Give the position of every malaria parasite.
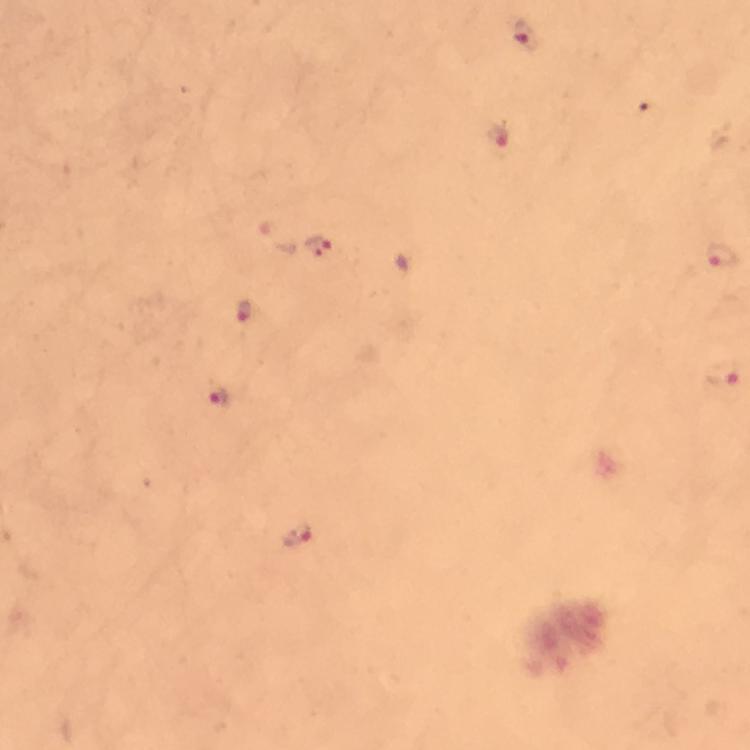

Approximate centers as {x, y} in pixels.
Malaria parasites: {526, 36}, {501, 138}, {319, 247}, {720, 253}, {243, 311}, {722, 374}, {218, 397}, {297, 535}.

cropped_from: one field of view
magnification: 100x
capture: smartphone camera through the microscope
image_size: 750×750 pixels
context: from a malaria diagnostic workup
immersion_oil: used
stain: Giemsa
preparation: thick blood smear